Identify the cell.
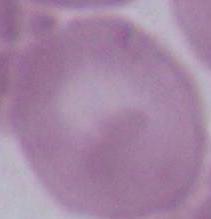
This is an erythrocyte.

Micrograph. 1000x magnification.